Assess the morphology of the red blood cells.
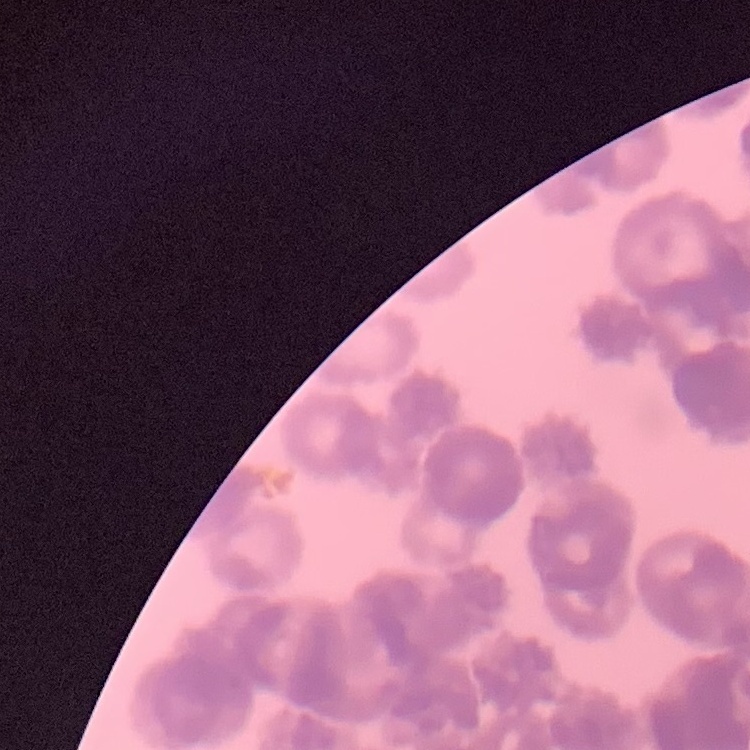
Rouleaux formation.

image type = one tile cut from a larger photomicrograph
preparation = thin blood film
stain = Field's or Giemsa